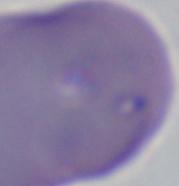
Summary:
  - Modality: micrograph
  - Magnification: 1000x
  - Identification: Babesia